Comment on the morphology of the erythrocytes.
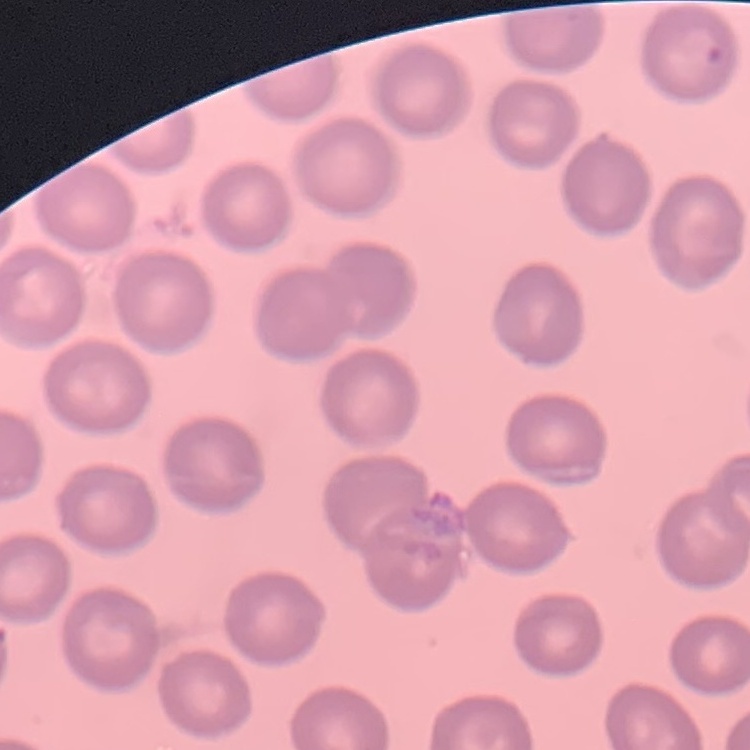

No rouleaux formation.

Thin peripheral smear. Stained with either Field's or Giemsa. One tile cut from a larger photomicrograph.